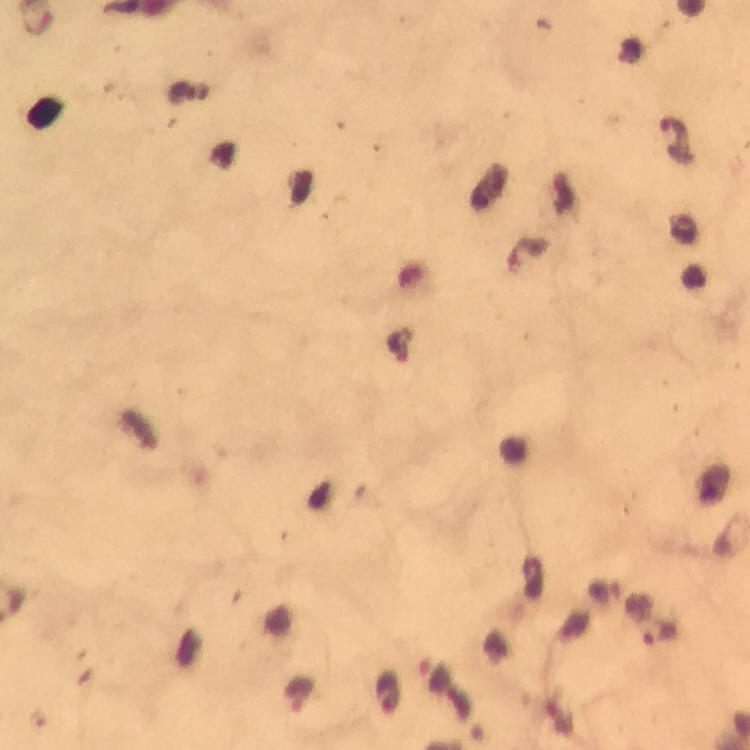
Approximate object centers, in pixels from the top-left corner.
Summary:
  - Malaria parasite locations: (x=673, y=131), (x=659, y=633), (x=386, y=693)
  - Capture: smartphone camera through the microscope
  - Context: from a malaria diagnostic workup
  - Image size: 750×750 pixels
  - Immersion oil: used
  - Stain: Giemsa
  - Preparation: thick blood film
  - Magnification: 100x
  - Cropped from: a single field of view